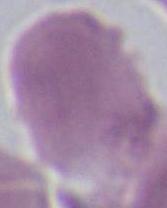

identification = red blood cell
modality = photomicrograph
magnification = 1000x